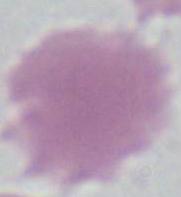

Summary:
  - Magnification: 1000x
  - Modality: micrograph
  - Identification: erythrocyte